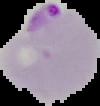 From a thin blood smear. Result: malaria parasites identified. Cell region segmented out of the field of view; the surrounding area is masked to black. Image is 100×106 pixels.